Report the malaria status of this cell.
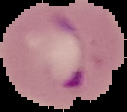
It is parasitized.

The area outside the segmented cell region is set to black. Image is 127×112 pixels. From a thin blood film.